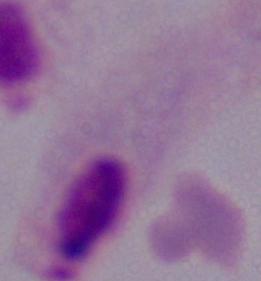

magnification: 1000x
identification: trichomonad
modality: micrograph